Outline each uninfected red blood cell.
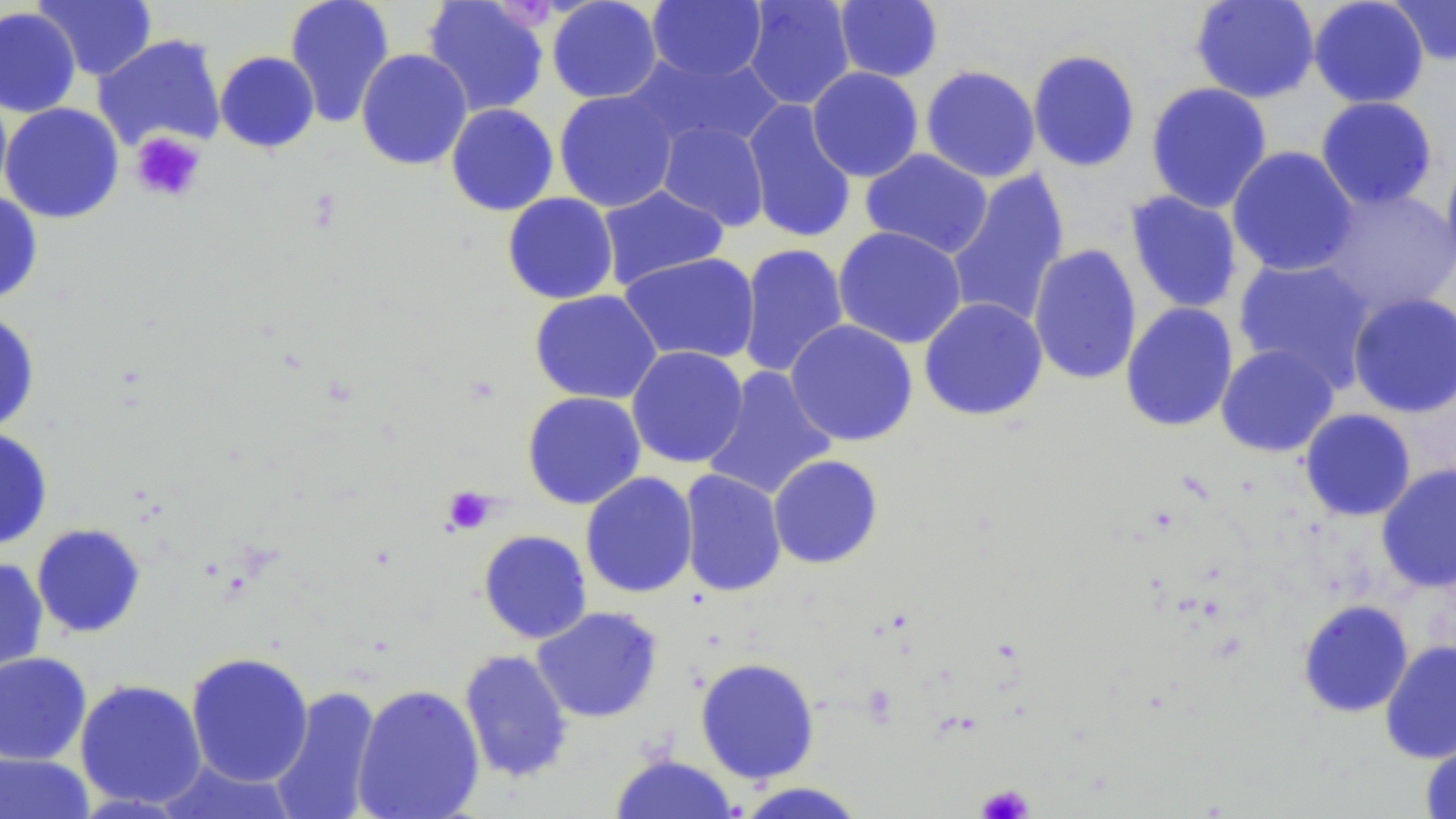

Approximate bounding boxes as (x1, y1, x2, y2) in pixels.
Uninfected red blood cells: (33, 0, 157, 81), (284, 0, 395, 128), (421, 0, 549, 117), (546, 0, 663, 103), (742, 0, 855, 110), (1190, 0, 1320, 103), (1308, 0, 1430, 109), (1387, 0, 1456, 66), (647, 1, 767, 82), (834, 1, 944, 83), (0, 6, 81, 117), (93, 34, 227, 152), (355, 48, 473, 170), (1027, 49, 1141, 173), (215, 51, 320, 154), (624, 51, 784, 153), (920, 65, 1041, 183), (807, 66, 924, 182), (1145, 81, 1273, 214), (0, 85, 13, 205), (553, 89, 679, 213), (1315, 96, 1439, 210), (742, 99, 858, 244), (0, 103, 124, 224), (445, 103, 559, 216), (657, 120, 769, 232), (1226, 146, 1358, 277), (860, 148, 993, 258), (1440, 151, 1456, 276), (946, 169, 1070, 329), (597, 185, 729, 291), (1316, 186, 1456, 316), (1124, 190, 1243, 314), (0, 191, 43, 305), (502, 192, 619, 304), (832, 226, 968, 350), (737, 243, 849, 379), (1027, 243, 1142, 386), (619, 252, 760, 364), (1233, 257, 1376, 391), (529, 290, 662, 405), (1347, 293, 1456, 418), (918, 297, 1048, 421), (1120, 302, 1239, 432), (0, 309, 40, 435), (785, 319, 918, 447), (1215, 343, 1339, 457), (626, 346, 749, 468), (702, 367, 837, 500), (522, 391, 646, 509), (1299, 408, 1417, 521), (0, 427, 53, 551), (768, 454, 884, 569), (1376, 463, 1456, 593), (678, 469, 787, 598), (580, 471, 698, 599), (31, 523, 146, 638), (478, 530, 592, 644), (0, 557, 49, 678), (1297, 599, 1414, 718), (531, 606, 663, 723), (1380, 640, 1456, 764), (458, 649, 574, 784), (0, 651, 93, 766), (185, 652, 314, 787), (695, 657, 820, 784), (74, 678, 207, 810), (352, 683, 485, 819), (268, 685, 383, 818), (1420, 734, 1456, 819), (0, 751, 95, 818), (609, 753, 740, 818), (156, 757, 298, 818), (732, 780, 870, 819).

{
  "slide_level_diagnosis": "negative for blood parasites",
  "magnification": "1000x",
  "platelet_locations": "approximate bounding boxes as (x1, y1, x2, y2) in pixels: (497, 3, 556, 33), (130, 131, 205, 203), (443, 486, 498, 534), (978, 784, 1033, 819)",
  "image_size": "1456×819 pixels",
  "preparation": "thin blood film",
  "field_of_view": "one of a larger specimen",
  "modality": "light microscopy",
  "stain": "May-Grünwald-Giemsa"
}